Describe the morphology of the red blood cells.
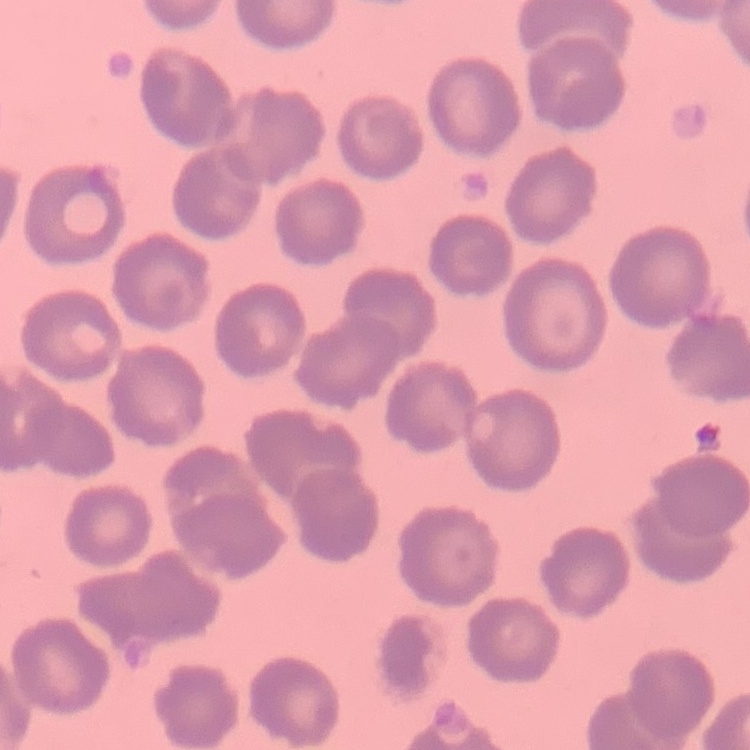
No rouleaux formation.

Summary:
  - Image type: square crop of a larger photomicrograph
  - Preparation: thin blood smear
  - Stain: Field's or Giemsa